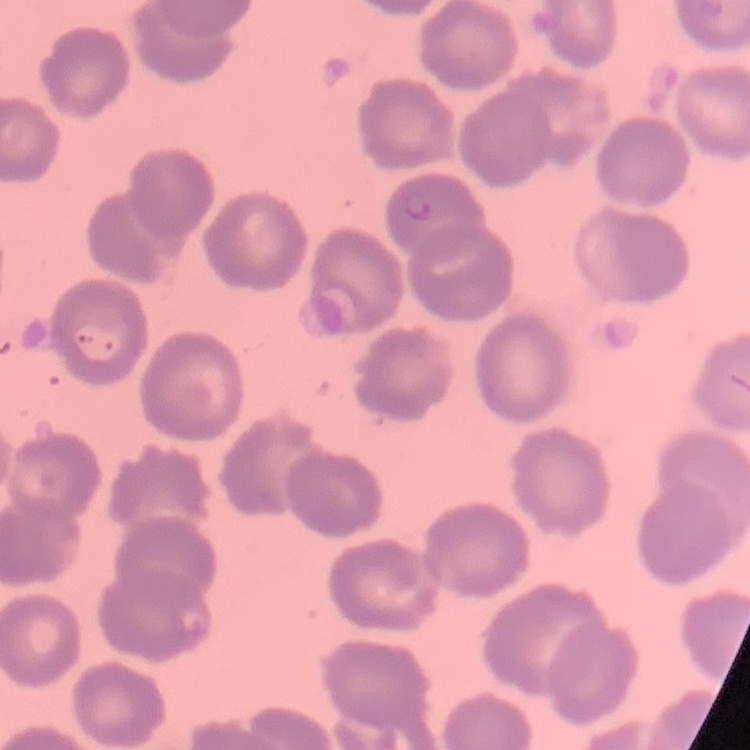

erythrocyte morphology = no rouleaux formation
image type = one tile cut from a larger photomicrograph
preparation = thin blood film
stain = Field's or Giemsa